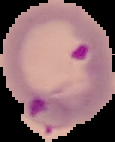

preparation = thin blood film
image size = 115×142 pixels
image type = segmented cell region with the area outside set to black
result = malaria parasites identified